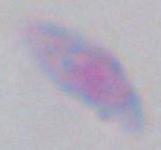

Summary:
  - Magnification: 1000x
  - Identification: Toxoplasma gondii
  - Modality: micrograph